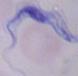
identification = trypanosome
magnification = 1000x
modality = micrograph